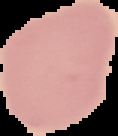
Summary:
  - Result: no Plasmodium parasites detected
  - Image size: 118×136 pixels
  - Preparation: thin blood smear
  - Image type: cell region segmented out of the field of view; surrounding area masked to black